Classify the preparation.
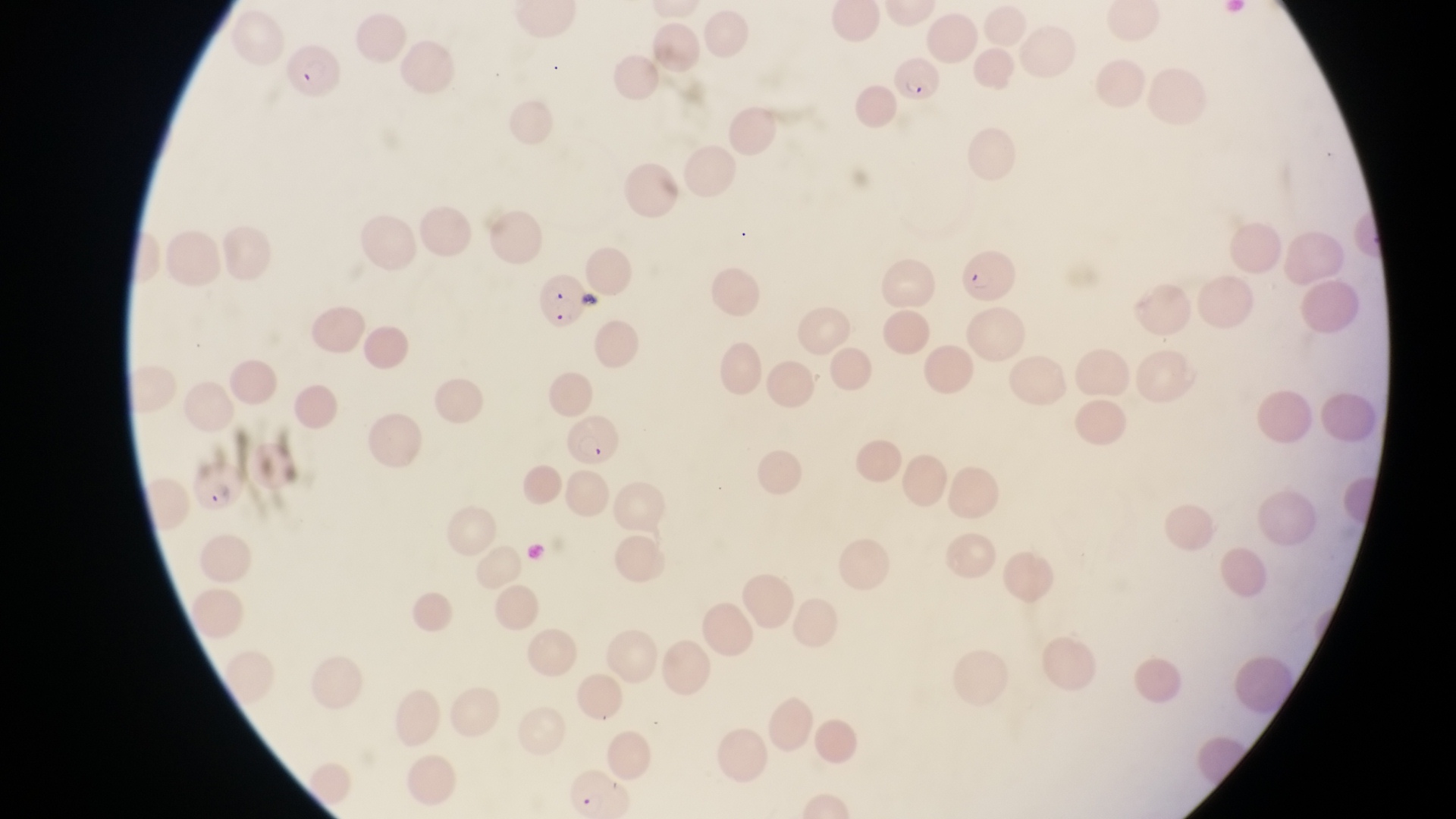

This is a thin smear.

field of view = single
capture = smartphone photograph through the eyepiece of an Olympus CX-23 microscope
parasitised red blood cell locations = approximate bounding boxes as [left, top, right, bottom] in pixels: [283, 46, 347, 101], [888, 60, 943, 109], [959, 251, 1020, 304], [534, 268, 590, 331], [566, 417, 625, 475], [188, 459, 247, 512]
magnification = 1000x
country = Uganda
image size = 1456×819 pixels